Locate every Plasmodium parasite.
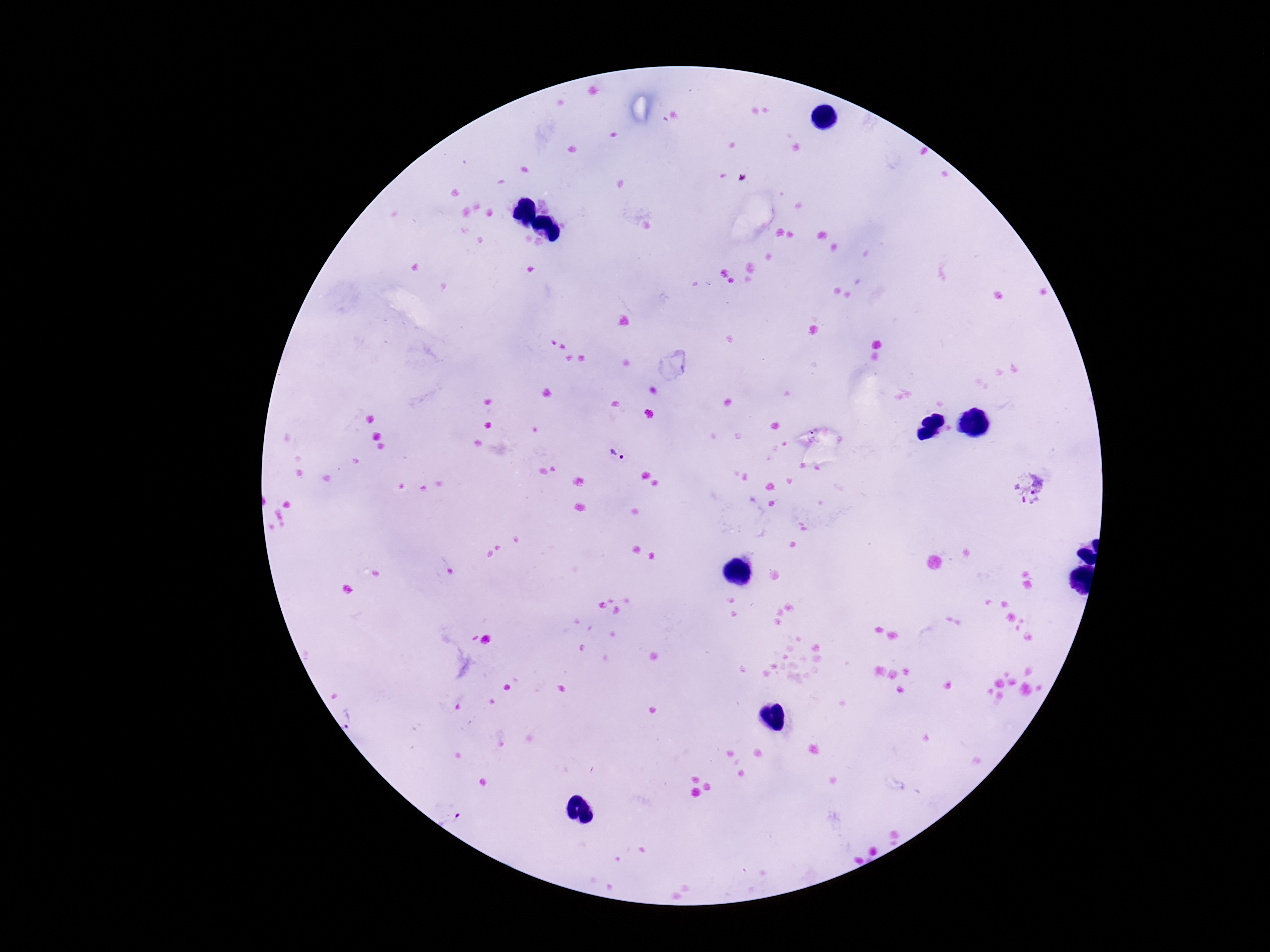

Approximate centers as {x, y} in pixels.
Plasmodium parasites: {618, 454}, {1030, 489}.

Giemsa stain. Thick blood film. Image is 1270×952 pixels. Patient malaria status: infected. Single field of view. Smartphone photograph taken through the microscope eyepiece. 100x magnification.